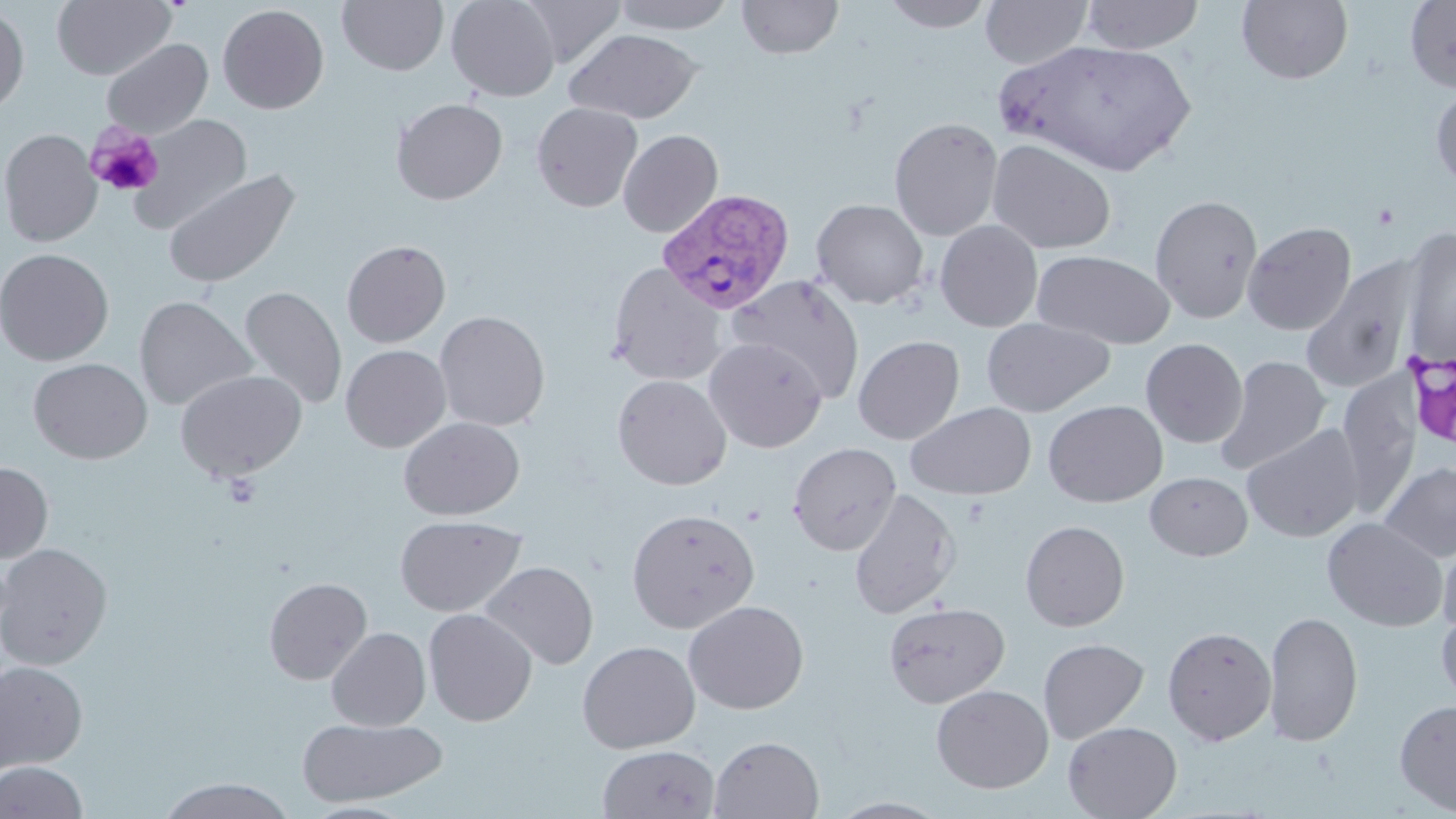
slide-level diagnosis = Plasmodium vivax
stain = May-Grünwald-Giemsa
magnification = 1000x
field of view = single
Plasmodium vivax-infected red blood cell locations = approximate bounding boxes as [x1, y1, x2, y2] in pixels: [656, 188, 795, 315]
modality = optical microscopy
image size = 1456×819 pixels
platelet locations = approximate bounding boxes as [x1, y1, x2, y2] in pixels: [86, 124, 164, 198]
uninfected red blood cell locations = approximate bounding boxes as [x1, y1, x2, y2] in pixels: [52, 0, 176, 80], [337, 0, 448, 75], [447, 0, 559, 101], [520, 0, 627, 67], [611, 0, 736, 33], [737, 0, 843, 59], [882, 0, 995, 32], [980, 0, 1093, 69], [1081, 0, 1204, 54], [1236, 0, 1353, 84], [1404, 1, 1456, 92], [217, 4, 329, 114], [0, 5, 29, 116], [566, 28, 702, 123], [101, 38, 213, 139], [997, 38, 1197, 176], [1430, 83, 1456, 193], [391, 98, 508, 204], [531, 102, 643, 212], [129, 114, 252, 234], [888, 117, 1003, 241], [0, 128, 102, 247], [618, 129, 724, 237], [986, 138, 1117, 255], [163, 168, 300, 289], [1149, 194, 1263, 323], [811, 198, 929, 308], [935, 220, 1043, 332], [1242, 221, 1356, 335], [1400, 228, 1456, 365], [342, 240, 451, 348], [0, 248, 114, 365], [1033, 249, 1175, 350], [1301, 257, 1420, 395], [607, 261, 727, 386], [727, 274, 866, 402], [239, 286, 347, 410], [134, 296, 257, 410], [434, 311, 551, 432], [981, 317, 1114, 416], [853, 335, 964, 445], [703, 337, 828, 452], [1140, 338, 1248, 448], [340, 344, 451, 452], [1217, 356, 1331, 474], [29, 358, 152, 464], [174, 369, 308, 480], [612, 374, 731, 490], [1043, 400, 1168, 507], [905, 402, 1036, 500], [398, 416, 525, 521], [1242, 423, 1365, 543], [787, 442, 901, 555], [0, 461, 53, 563], [1379, 461, 1456, 563], [1145, 471, 1252, 561], [848, 488, 961, 619], [626, 508, 760, 633], [395, 515, 526, 617], [1321, 516, 1449, 632], [1020, 519, 1130, 632], [1437, 530, 1456, 639], [0, 543, 113, 670], [478, 561, 599, 670], [263, 576, 372, 684], [683, 600, 809, 714], [884, 602, 1010, 707], [1437, 607, 1456, 708], [423, 608, 537, 726], [1263, 610, 1363, 747], [1162, 626, 1277, 746], [326, 627, 431, 731], [1038, 638, 1149, 744], [577, 640, 700, 753], [1, 661, 88, 771], [931, 684, 1053, 793], [1394, 698, 1456, 814], [297, 716, 447, 807], [1063, 721, 1182, 819], [708, 735, 825, 819], [597, 744, 720, 819], [0, 760, 88, 819], [157, 778, 297, 818], [827, 797, 952, 818]
preparation = thin blood film